Describe the morphology of the erythrocytes.
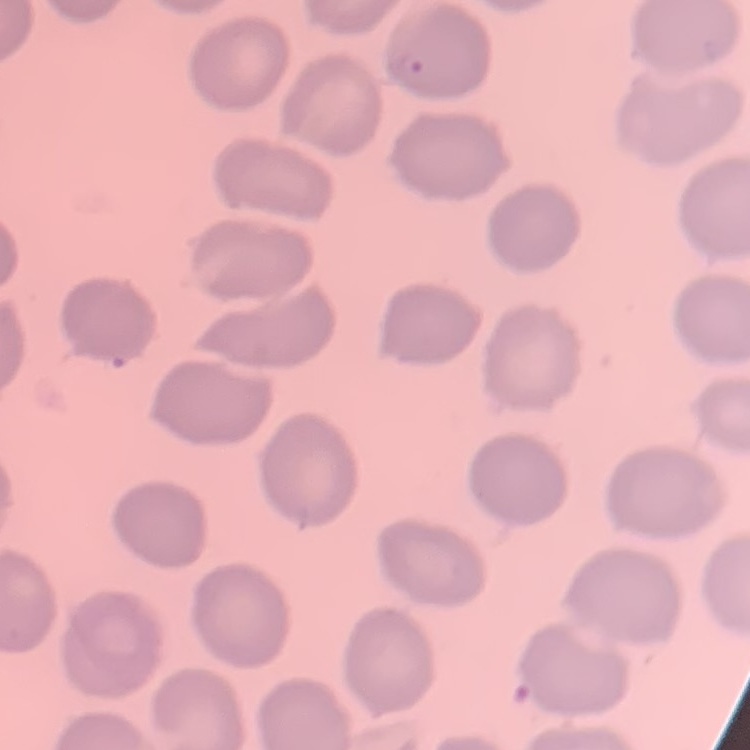

No rouleaux formation.

{
  "preparation": "thin blood film",
  "stain": "Field's or Giemsa",
  "image_type": "square crop of a larger photomicrograph"
}